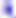
Summary:
  - Magnification: 400x
  - Modality: photomicrograph
  - Identification: Toxoplasma gondii